State which cell type is depicted.
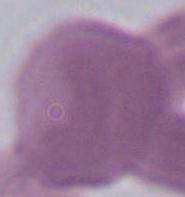

An erythrocyte.

Summary:
  - Magnification: 1000x
  - Modality: micrograph